Assess the morphology of the erythrocytes.
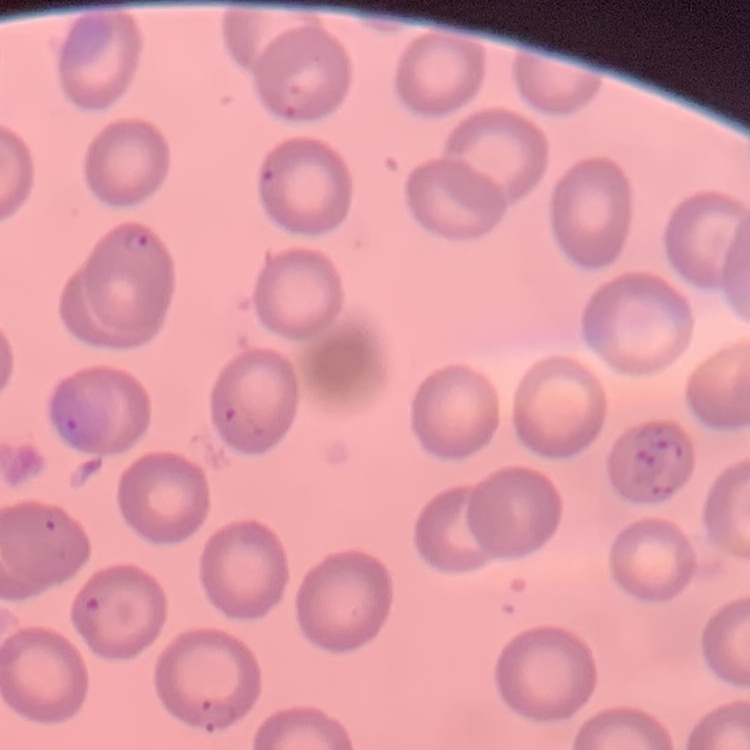
No rouleaux formation.

Summary:
  - Stain: Field's or Giemsa
  - Image type: one tile cut from a larger photomicrograph
  - Preparation: thin peripheral smear